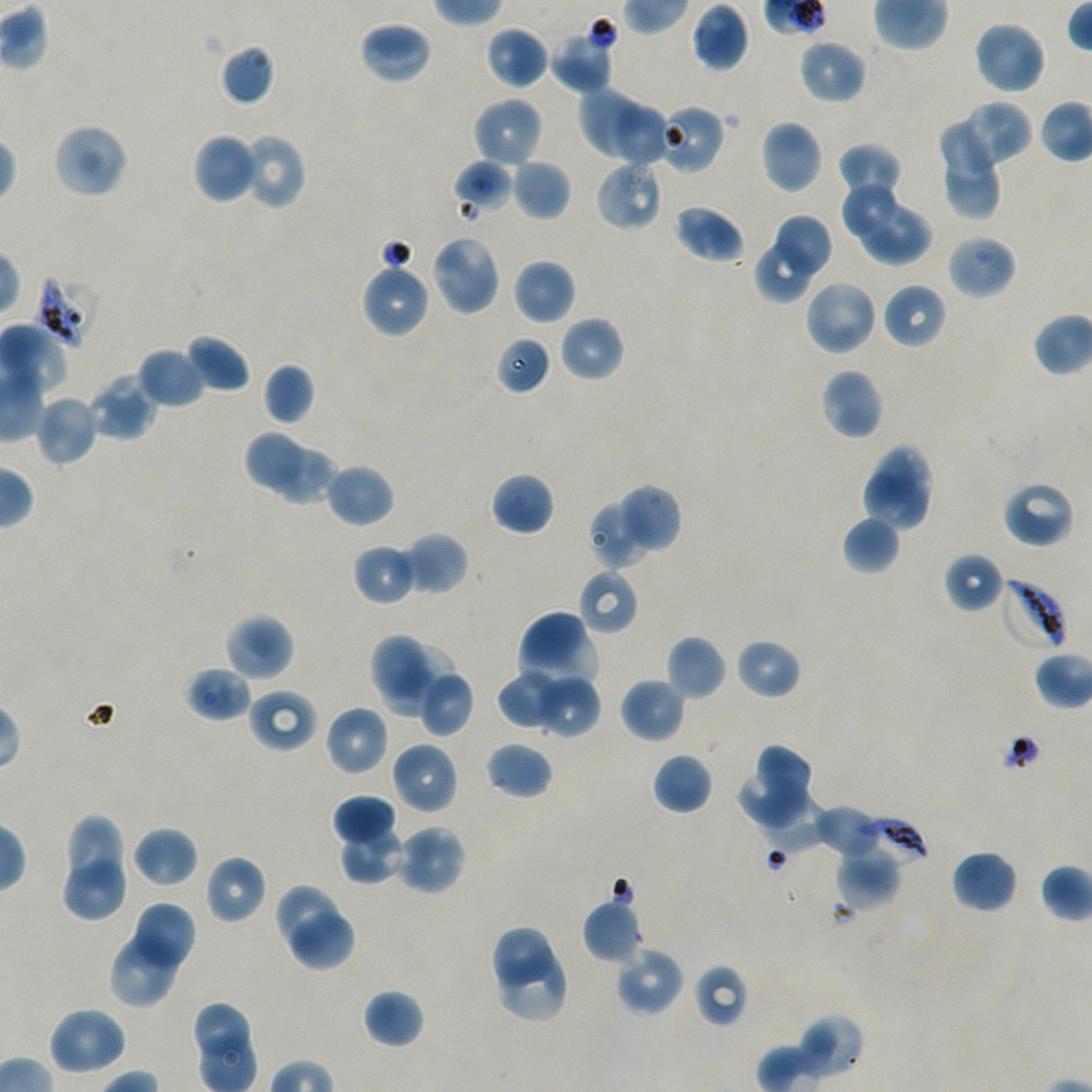

Approximate bounding rectangles given as corner coordinates in pixels from the top-left. Not every red blood cell is marked.
Summary:
  - Locations of infected red blood cells: (x1=35, y1=274, x2=100, y2=347), (x1=998, y1=577, x2=1069, y2=653), (x1=857, y1=818, x2=930, y2=865)
  - Locations of red blood cells of indeterminate infection status: (x1=661, y1=105, x2=726, y2=174), (x1=946, y1=234, x2=1017, y2=300), (x1=693, y1=963, x2=748, y2=1027)
  - Locations of uninfected red blood cells: (x1=691, y1=1, x2=749, y2=71), (x1=972, y1=20, x2=1047, y2=95), (x1=359, y1=21, x2=433, y2=85), (x1=484, y1=26, x2=549, y2=91), (x1=550, y1=29, x2=616, y2=94), (x1=798, y1=38, x2=867, y2=104), (x1=217, y1=43, x2=275, y2=107), (x1=576, y1=86, x2=644, y2=164), (x1=471, y1=97, x2=543, y2=168), (x1=960, y1=99, x2=1034, y2=167), (x1=612, y1=102, x2=667, y2=168), (x1=939, y1=117, x2=994, y2=181), (x1=759, y1=120, x2=823, y2=194), (x1=52, y1=122, x2=129, y2=199), (x1=239, y1=132, x2=307, y2=211), (x1=192, y1=133, x2=261, y2=204), (x1=837, y1=142, x2=903, y2=202), (x1=943, y1=156, x2=1004, y2=221), (x1=453, y1=159, x2=513, y2=215), (x1=511, y1=159, x2=571, y2=221), (x1=595, y1=160, x2=663, y2=231), (x1=841, y1=184, x2=899, y2=235), (x1=856, y1=202, x2=933, y2=265), (x1=673, y1=204, x2=746, y2=264), (x1=777, y1=213, x2=833, y2=275), (x1=431, y1=234, x2=502, y2=316), (x1=755, y1=242, x2=813, y2=302), (x1=513, y1=259, x2=575, y2=325), (x1=360, y1=261, x2=431, y2=338), (x1=804, y1=278, x2=879, y2=357), (x1=882, y1=283, x2=947, y2=350), (x1=558, y1=316, x2=625, y2=382), (x1=185, y1=333, x2=251, y2=394), (x1=496, y1=336, x2=551, y2=395), (x1=137, y1=346, x2=208, y2=410), (x1=263, y1=363, x2=316, y2=426), (x1=820, y1=368, x2=884, y2=440), (x1=87, y1=373, x2=158, y2=442), (x1=34, y1=394, x2=100, y2=467), (x1=243, y1=430, x2=302, y2=490), (x1=860, y1=443, x2=935, y2=532), (x1=268, y1=450, x2=341, y2=506), (x1=325, y1=462, x2=395, y2=528), (x1=490, y1=471, x2=554, y2=536), (x1=1001, y1=481, x2=1076, y2=548), (x1=613, y1=484, x2=683, y2=557), (x1=587, y1=496, x2=657, y2=570), (x1=842, y1=515, x2=901, y2=575), (x1=402, y1=532, x2=469, y2=596), (x1=352, y1=543, x2=418, y2=606), (x1=943, y1=551, x2=1005, y2=613), (x1=577, y1=568, x2=639, y2=636), (x1=517, y1=611, x2=597, y2=687), (x1=223, y1=613, x2=294, y2=681), (x1=370, y1=634, x2=431, y2=696), (x1=666, y1=634, x2=727, y2=701), (x1=735, y1=638, x2=801, y2=700), (x1=380, y1=642, x2=456, y2=719), (x1=184, y1=666, x2=252, y2=722), (x1=417, y1=668, x2=474, y2=737), (x1=496, y1=670, x2=568, y2=731), (x1=535, y1=675, x2=602, y2=739), (x1=619, y1=677, x2=686, y2=744), (x1=247, y1=689, x2=318, y2=752), (x1=324, y1=704, x2=389, y2=776), (x1=390, y1=741, x2=459, y2=815), (x1=485, y1=742, x2=553, y2=800), (x1=755, y1=746, x2=810, y2=797), (x1=653, y1=752, x2=713, y2=815), (x1=737, y1=774, x2=806, y2=831), (x1=331, y1=793, x2=397, y2=850), (x1=759, y1=793, x2=828, y2=854), (x1=814, y1=803, x2=885, y2=858), (x1=67, y1=814, x2=124, y2=886), (x1=338, y1=823, x2=406, y2=885), (x1=395, y1=825, x2=467, y2=895), (x1=132, y1=826, x2=198, y2=886), (x1=835, y1=850, x2=901, y2=910), (x1=950, y1=850, x2=1019, y2=914), (x1=204, y1=854, x2=267, y2=924), (x1=65, y1=858, x2=124, y2=923), (x1=274, y1=883, x2=338, y2=950), (x1=582, y1=899, x2=641, y2=964), (x1=134, y1=901, x2=197, y2=968), (x1=291, y1=913, x2=354, y2=971), (x1=109, y1=925, x2=184, y2=1010), (x1=492, y1=928, x2=554, y2=990), (x1=614, y1=945, x2=685, y2=1016), (x1=500, y1=947, x2=568, y2=1022), (x1=363, y1=988, x2=425, y2=1050), (x1=47, y1=1006, x2=128, y2=1076), (x1=794, y1=1013, x2=864, y2=1079)
  - Preparation: thin blood film
  - Field of view: single
  - Image size: 1092×1092 pixels
  - Objective: 100x, oil immersion, numerical aperture 1.45
  - Stain: Giemsa
  - Donor blood group: A+/O+
  - Culture: static in-vitro Plasmodium falciparum strain NF54